Locate every blood parasite and identify its species.
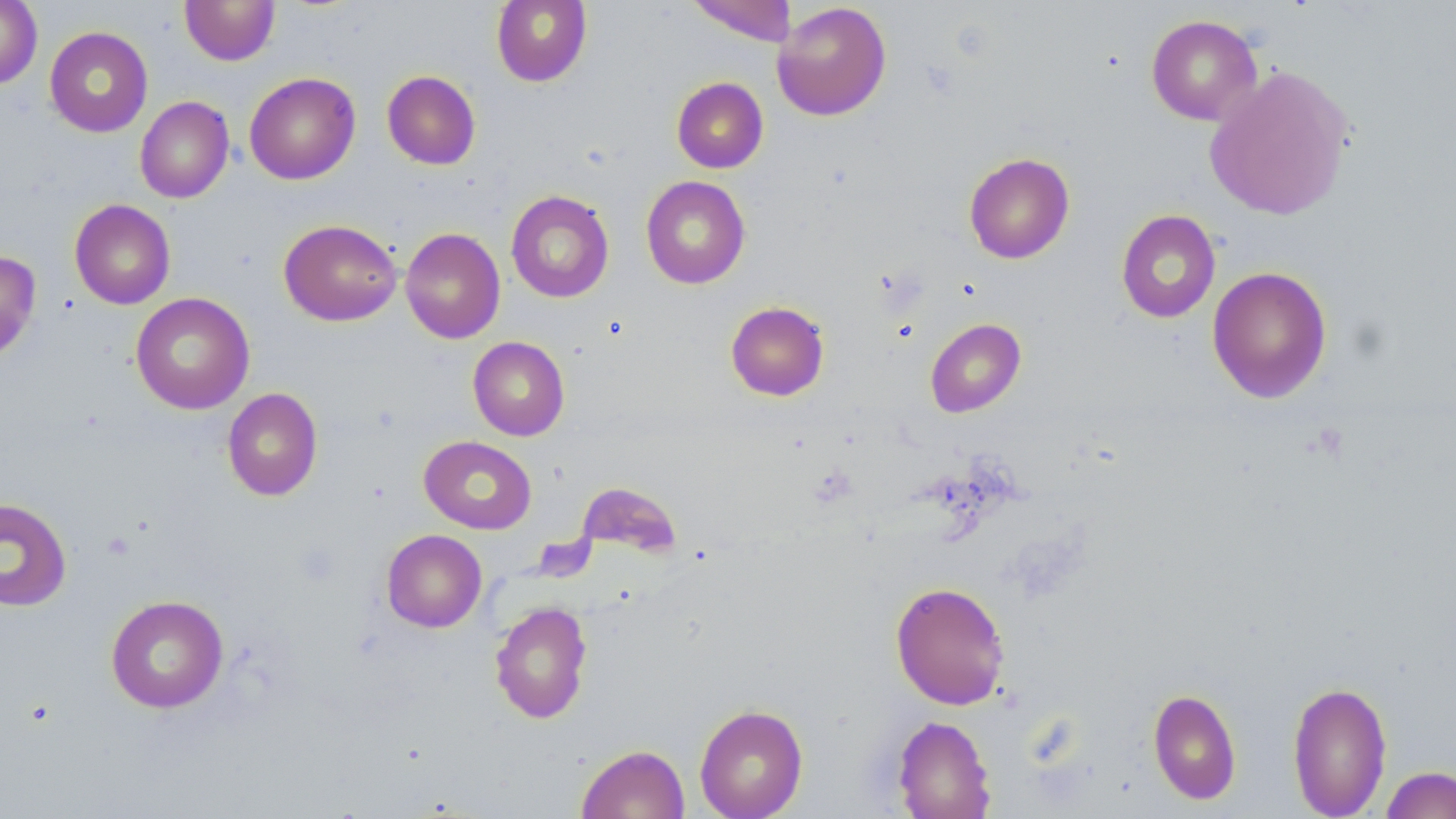

No blood parasites observed.

Approximate bounding boxes as (x1,y1)-(x2,y2) corner pairs in pixels. Uninfected red blood cell locations: (179,0)-(280,66), (491,0)-(592,87), (687,0)-(797,46), (0,1)-(42,89), (772,2)-(891,121), (1146,14)-(1262,126), (44,26)-(153,137), (1203,63)-(1356,221), (382,70)-(481,170), (244,72)-(361,185), (672,77)-(768,173), (135,96)-(234,203), (963,152)-(1075,264), (641,175)-(751,289), (506,190)-(615,303), (69,199)-(175,309), (1116,209)-(1221,323), (279,219)-(402,326), (400,227)-(505,344), (0,249)-(41,363), (1207,266)-(1332,404), (130,292)-(255,415), (725,301)-(830,401), (925,318)-(1026,417), (468,336)-(569,440), (222,387)-(323,501), (419,435)-(537,534), (0,497)-(72,611), (381,529)-(487,632), (890,581)-(1011,710), (105,595)-(228,713), (490,600)-(593,724), (1287,680)-(1393,818), (1148,688)-(1241,805), (694,703)-(808,819), (891,715)-(996,819), (576,744)-(689,819), (1381,765)-(1456,819). Slide-level diagnosis: no evidence of blood parasites. May-Grünwald-Giemsa-stained preparation. One field of a larger specimen. Image is 1456×819 pixels. Thin blood film. 1000x magnification. Light microscopy.